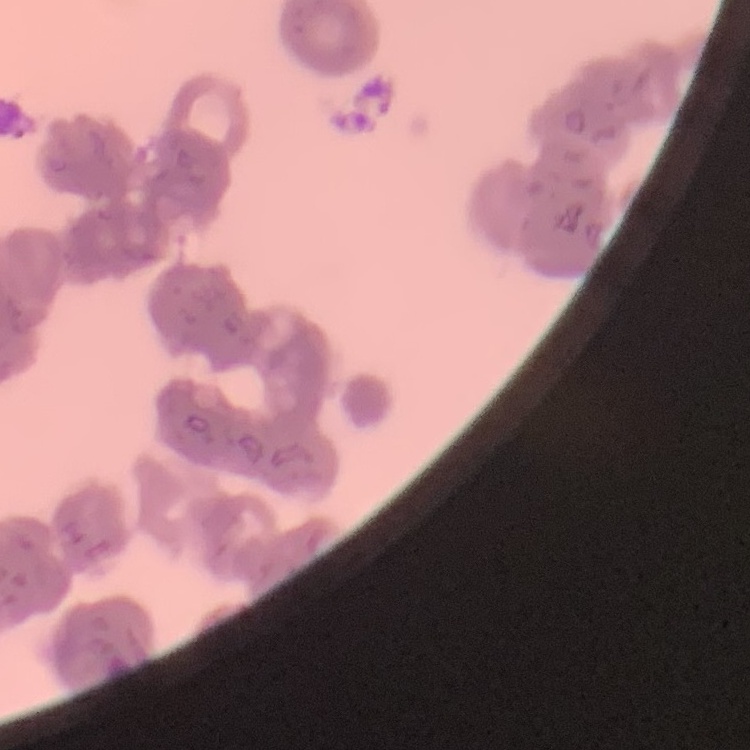

{
  "red_blood_cell_morphology": "rouleaux formation",
  "preparation": "thin blood film",
  "image_type": "square crop of a larger photomicrograph",
  "stain": "Field's or Giemsa"
}